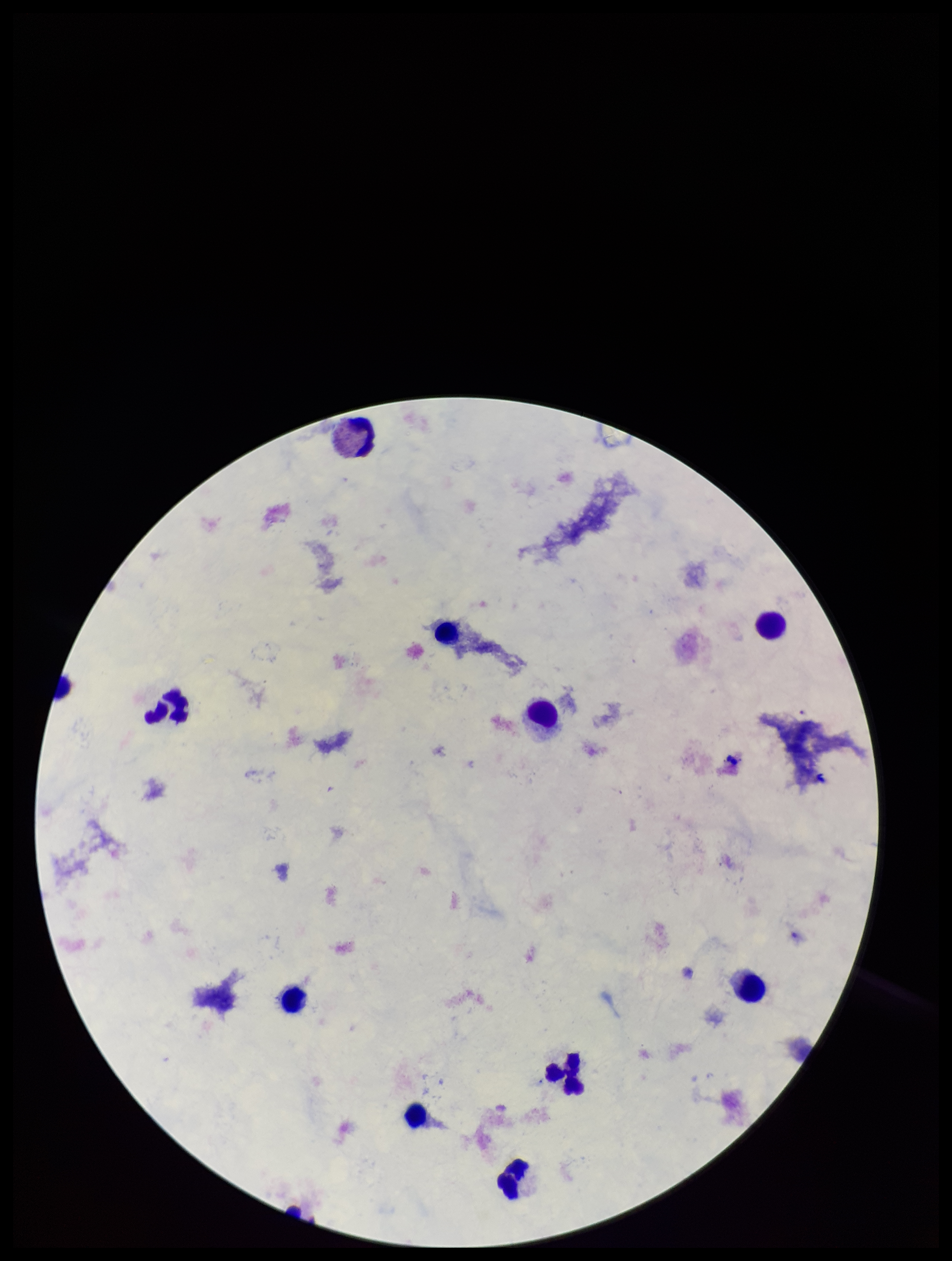
preparation: thick blood smear
field_of_view: one from this slide
parasite_count: 0
capture: smartphone photograph through the microscope eyepiece
stain: Giemsa
patient_malaria_status: negative
image_size: 952×1261 pixels
plasmodium_parasites: none identified
leukocyte_count: 11